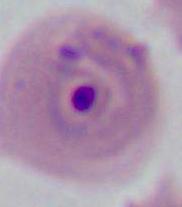
A Plasmodium parasite is seen. Micrograph. Captured at either 400x or 1000x magnification.